Locate and identify every blood parasite.
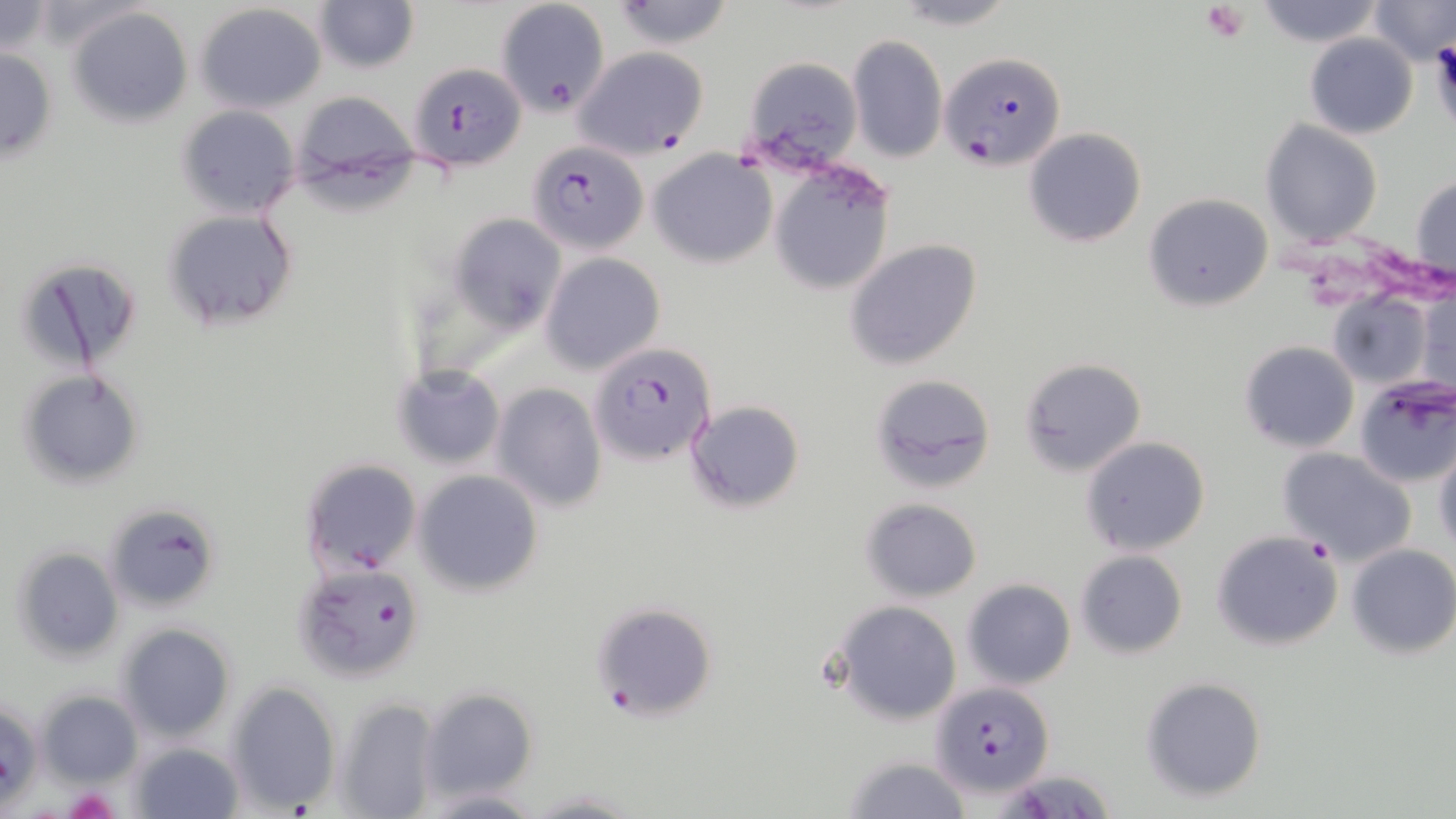
Approximate bounding boxes as [x1, y1, x2, y2] in pixels.
Plasmodium falciparum-infected red blood cells: [941, 53, 1064, 171], [408, 62, 526, 172], [527, 143, 648, 253], [590, 340, 718, 465], [292, 563, 424, 682], [591, 602, 719, 721], [931, 683, 1054, 799].
No Plasmodium ovale, Plasmodium malariae, Plasmodium vivax, Babesia divergens, or Trypanosoma brucei observed.

Uninfected red blood cell locations: [315, 0, 420, 72], [494, 0, 610, 120], [610, 0, 736, 49], [1253, 0, 1384, 49], [1365, 0, 1456, 66], [0, 1, 56, 58], [895, 1, 1018, 29], [195, 3, 328, 115], [68, 7, 192, 128], [846, 34, 946, 164], [1305, 34, 1416, 139], [0, 45, 57, 162], [574, 47, 707, 158], [742, 55, 864, 165], [294, 91, 422, 196], [178, 106, 299, 218], [1261, 120, 1382, 245], [1024, 128, 1146, 247], [648, 151, 775, 268], [770, 168, 895, 298], [1411, 174, 1455, 286], [1143, 192, 1274, 311], [161, 209, 299, 332], [448, 213, 566, 332], [845, 239, 983, 369], [542, 253, 665, 375], [13, 254, 146, 374], [1418, 288, 1454, 396], [1325, 289, 1436, 391], [1240, 340, 1359, 452], [1018, 357, 1146, 476], [392, 365, 505, 469], [19, 372, 144, 486], [868, 373, 996, 494], [1353, 378, 1456, 488], [492, 383, 608, 513], [684, 399, 805, 514], [1081, 436, 1209, 556], [1432, 446, 1456, 553], [1280, 448, 1416, 565], [300, 458, 422, 575], [413, 469, 545, 596], [861, 497, 982, 602], [104, 502, 221, 612], [1211, 529, 1344, 651], [1345, 544, 1456, 659], [10, 545, 124, 662], [1076, 550, 1188, 660], [962, 578, 1076, 689], [831, 602, 962, 724], [115, 623, 237, 742], [1140, 675, 1268, 803], [227, 682, 342, 812], [417, 686, 540, 801], [35, 689, 143, 786], [336, 696, 442, 819], [1, 700, 42, 810], [131, 741, 245, 818], [842, 756, 973, 818], [996, 767, 1117, 818], [416, 787, 545, 817], [525, 788, 640, 818]. Platelet locations: [1202, 2, 1251, 43], [1427, 44, 1456, 123], [64, 787, 120, 817]. Slide-level diagnosis: Plasmodium falciparum. Thin blood smear. One field of a larger specimen. Optical microscopy. May-Grünwald-Giemsa-stained preparation. Image is 1456×819 pixels. 1000x magnification.